Classify this cell by malaria status.
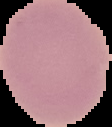

Uninfected.

{
  "image_type": "segmented cell region with the area outside set to black",
  "preparation": "thin blood film",
  "image_size": "112×127 pixels"
}